Identify the cell.
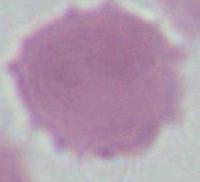

An erythrocyte.

Summary:
  - Modality: micrograph
  - Magnification: 1000x